Locate every Plasmodium parasite.
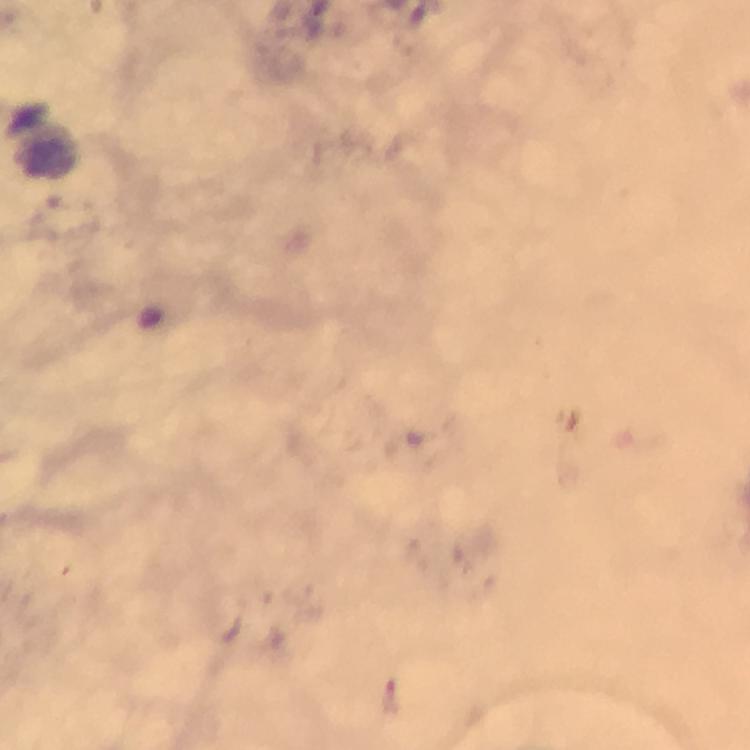
Approximate object centers, in pixels from the top-left corner.
Plasmodium parasites: (x=391, y=693).

Summary:
  - Immersion oil: used
  - Cropped from: one field of view
  - Preparation: thick blood smear
  - Magnification: 100x
  - Context: from a malaria diagnostic workup
  - Image size: 750×750 pixels
  - Stain: Giemsa
  - Capture: smartphone photograph through a microscope